State which parasite is depicted.
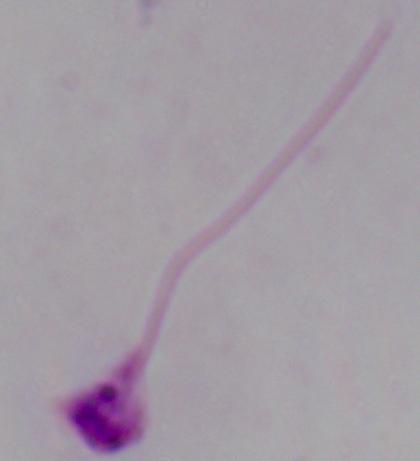

This is Leishmania.

{
  "modality": "micrograph",
  "magnification": "1000x"
}